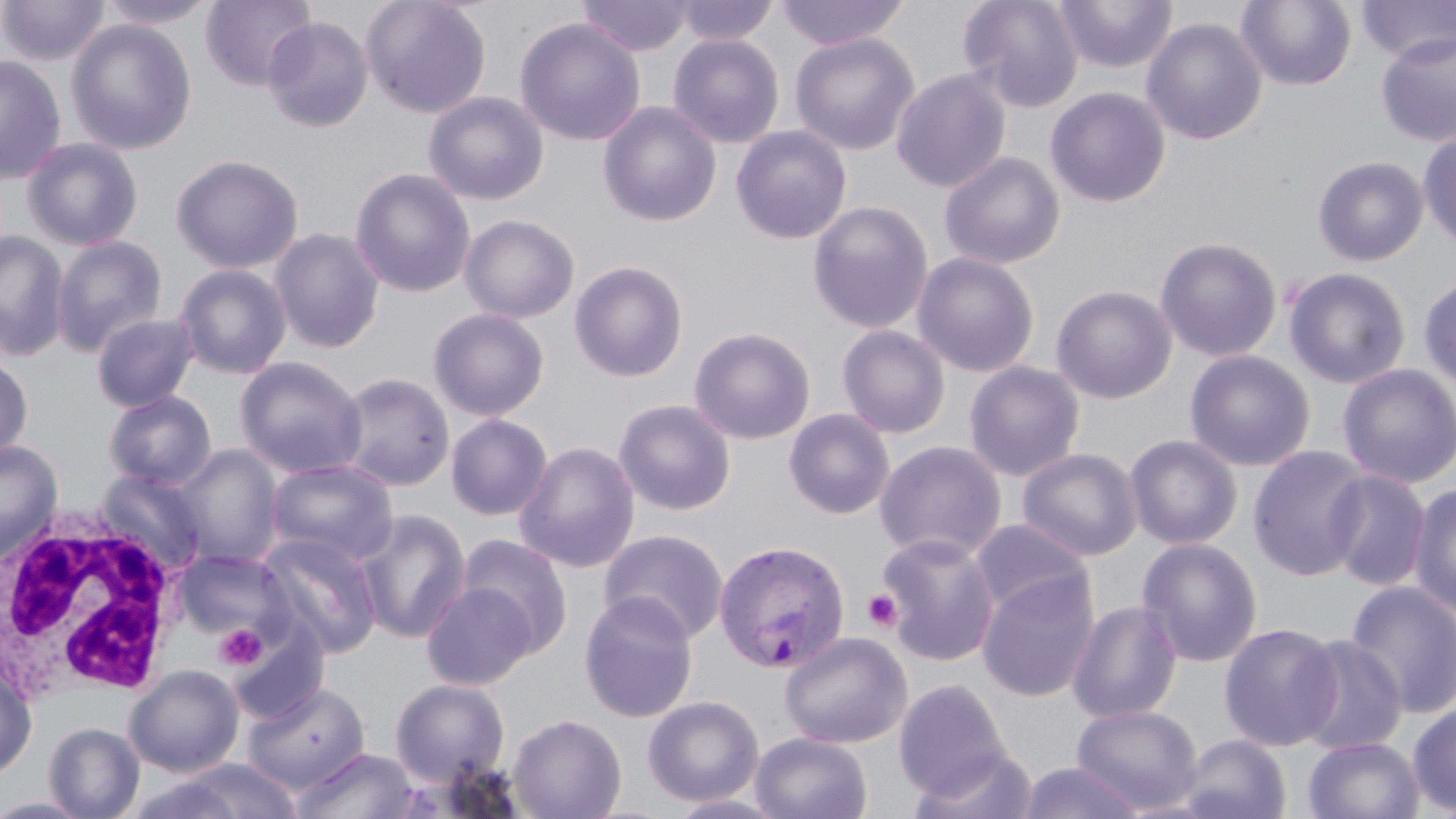 Approximate bounding boxes as (x1, y1, x2, y2) in pixels. Plasmodium vivax-infected red blood cell locations: (713, 539, 850, 673). White blood cell locations: (3, 502, 191, 703). Platelet locations: (862, 589, 903, 632), (213, 622, 268, 671). Uninfected red blood cell locations: (0, 0, 110, 67), (98, 0, 221, 29), (200, 0, 319, 92), (360, 0, 492, 118), (577, 0, 694, 57), (673, 0, 779, 46), (774, 0, 911, 50), (957, 0, 1084, 112), (1052, 0, 1178, 74), (1236, 0, 1357, 91), (1356, 1, 1456, 64), (262, 16, 374, 133), (1141, 16, 1267, 146), (514, 17, 646, 146), (65, 19, 197, 155), (1375, 30, 1456, 148), (789, 33, 920, 155), (668, 34, 785, 148), (0, 54, 67, 185), (891, 68, 1011, 193), (1045, 86, 1170, 208), (423, 91, 548, 206), (597, 101, 722, 227), (731, 124, 852, 244), (1417, 127, 1456, 251), (21, 137, 144, 251), (938, 151, 1065, 270), (170, 153, 304, 274), (1313, 155, 1429, 267), (350, 168, 476, 298), (807, 201, 934, 334), (459, 214, 580, 324), (268, 227, 385, 354), (0, 230, 70, 361), (51, 235, 168, 357), (1154, 236, 1282, 362), (912, 252, 1040, 377), (569, 260, 689, 382), (174, 263, 292, 379), (1283, 267, 1412, 389), (1418, 272, 1456, 390), (1050, 284, 1177, 404), (428, 308, 550, 421), (91, 312, 200, 412), (837, 324, 951, 439), (688, 326, 816, 444), (1184, 350, 1316, 472), (0, 351, 34, 464), (235, 356, 367, 478), (963, 360, 1085, 481), (1337, 364, 1455, 488), (335, 372, 455, 491), (104, 390, 217, 490), (613, 399, 737, 515), (784, 408, 895, 519), (446, 414, 552, 520), (1124, 434, 1243, 550), (0, 440, 63, 561), (874, 440, 1007, 562), (514, 441, 641, 573), (172, 444, 284, 568), (1248, 445, 1372, 581), (1017, 447, 1142, 561), (266, 458, 397, 565), (1324, 469, 1430, 591), (97, 470, 208, 574), (1408, 482, 1456, 617), (352, 510, 472, 644), (970, 518, 1093, 620), (599, 529, 729, 644), (257, 531, 383, 658), (876, 532, 1001, 666), (456, 533, 573, 657), (1136, 537, 1263, 668), (172, 549, 291, 643), (976, 569, 1100, 703), (1344, 580, 1456, 719), (421, 581, 538, 691), (578, 592, 700, 724), (1067, 599, 1182, 722), (227, 619, 330, 725), (1219, 622, 1342, 751), (779, 631, 912, 748), (1291, 634, 1408, 756), (0, 664, 37, 779), (124, 665, 245, 777), (390, 678, 510, 787), (893, 678, 1011, 800), (242, 682, 371, 795), (642, 695, 764, 807), (1072, 704, 1203, 814), (1407, 704, 1456, 815), (508, 713, 627, 819), (43, 722, 144, 818), (751, 732, 872, 818), (1177, 733, 1292, 819), (1303, 737, 1424, 819), (911, 746, 1038, 819), (291, 747, 420, 819), (157, 759, 306, 818), (1016, 761, 1146, 819), (667, 793, 790, 818), (0, 796, 97, 818). Slide-level diagnosis: Plasmodium vivax. Optical microscopy. May-Grünwald-Giemsa-stained preparation. Single field of view. Thin blood film. 1000x magnification. Image is 1456×819 pixels.